Locate every malaria parasite.
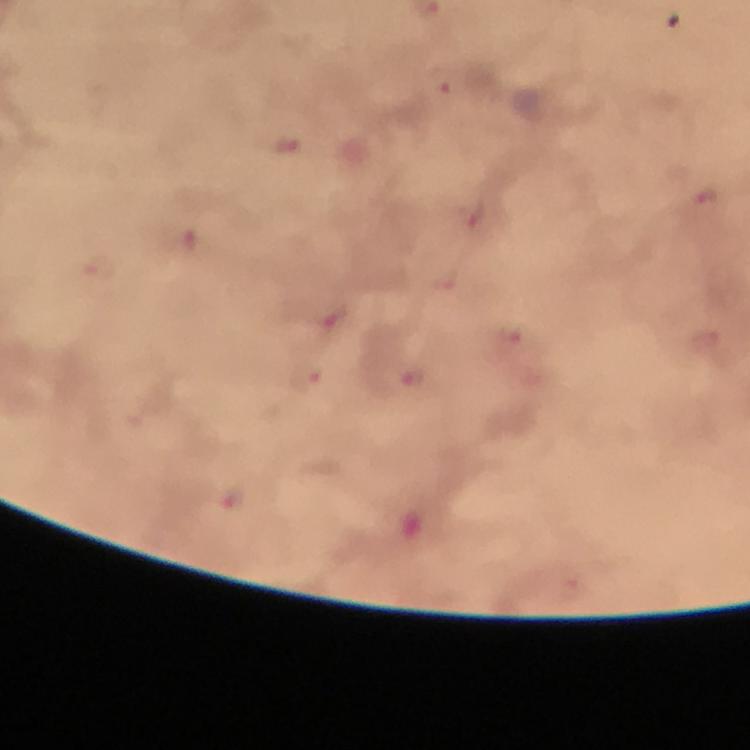

Approximate centers as (x, y) in pixels.
Malaria parasites: (444, 82), (289, 145), (706, 198), (471, 215), (188, 240), (98, 271), (337, 316), (510, 339), (304, 377), (407, 378), (233, 499).

Summary:
  - Immersion oil: used
  - Context: from a malaria diagnostic workup
  - Magnification: 100x
  - Cropped from: a single field of view
  - Image size: 750×750 pixels
  - Stain: Giemsa
  - Preparation: thick blood film
  - Capture: smartphone photograph through a microscope